Report the malaria status of this cell.
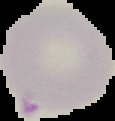
It is parasitized.

From a thin blood film. Image is 115×121 pixels. The area outside the segmented cell region is set to black.